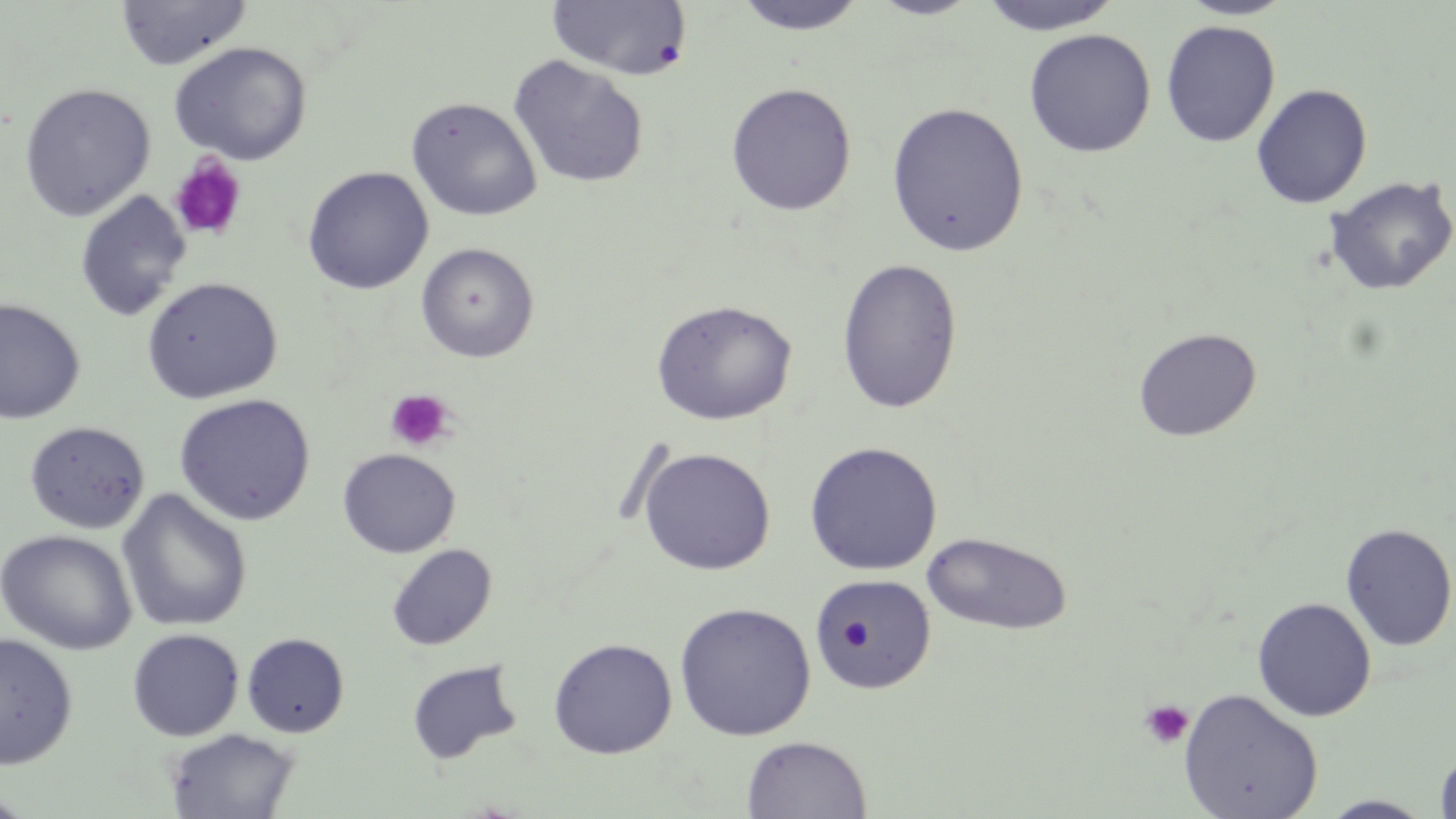

Approximate bounding boxes as named x1/y1/x2/y2 corners in pixels. Uninfected red blood cell locations: (x1=115, y1=0, x2=251, y2=70), (x1=731, y1=0, x2=869, y2=35), (x1=866, y1=0, x2=985, y2=20), (x1=977, y1=0, x2=1124, y2=36), (x1=1176, y1=0, x2=1296, y2=20), (x1=547, y1=1, x2=692, y2=80), (x1=1160, y1=20, x2=1280, y2=148), (x1=1023, y1=28, x2=1156, y2=158), (x1=168, y1=41, x2=313, y2=165), (x1=508, y1=55, x2=649, y2=189), (x1=19, y1=82, x2=156, y2=221), (x1=725, y1=82, x2=857, y2=216), (x1=1251, y1=83, x2=1373, y2=209), (x1=405, y1=96, x2=543, y2=221), (x1=886, y1=101, x2=1030, y2=257), (x1=302, y1=166, x2=434, y2=295), (x1=1323, y1=175, x2=1456, y2=297), (x1=74, y1=190, x2=192, y2=323), (x1=415, y1=242, x2=539, y2=363), (x1=836, y1=258, x2=964, y2=415), (x1=141, y1=276, x2=283, y2=404), (x1=0, y1=298, x2=86, y2=424), (x1=650, y1=298, x2=798, y2=426), (x1=1132, y1=328, x2=1262, y2=442), (x1=174, y1=393, x2=316, y2=526), (x1=24, y1=420, x2=150, y2=534), (x1=803, y1=441, x2=942, y2=576), (x1=638, y1=447, x2=776, y2=575), (x1=337, y1=448, x2=460, y2=559), (x1=117, y1=488, x2=253, y2=633), (x1=1339, y1=523, x2=1456, y2=651), (x1=0, y1=529, x2=138, y2=655), (x1=921, y1=531, x2=1074, y2=636), (x1=386, y1=543, x2=497, y2=651), (x1=810, y1=573, x2=936, y2=695), (x1=1252, y1=596, x2=1377, y2=722), (x1=674, y1=602, x2=816, y2=741), (x1=127, y1=628, x2=245, y2=741), (x1=0, y1=631, x2=78, y2=769), (x1=241, y1=632, x2=350, y2=737), (x1=547, y1=637, x2=678, y2=759), (x1=405, y1=659, x2=523, y2=765), (x1=1179, y1=688, x2=1324, y2=819), (x1=164, y1=727, x2=301, y2=819), (x1=742, y1=735, x2=871, y2=819), (x1=1434, y1=748, x2=1456, y2=818), (x1=1318, y1=795, x2=1436, y2=818). Platelet locations: (x1=168, y1=154, x2=247, y2=242), (x1=385, y1=389, x2=455, y2=452), (x1=1139, y1=700, x2=1194, y2=749). Slide-level diagnosis: no evidence of blood parasites. Image is 1456×819 pixels. One field of a larger specimen. Optical microscopy. May-Grünwald-Giemsa stain. Thin blood smear. Captured at 1000x magnification.